Assess the morphology of the erythrocytes.
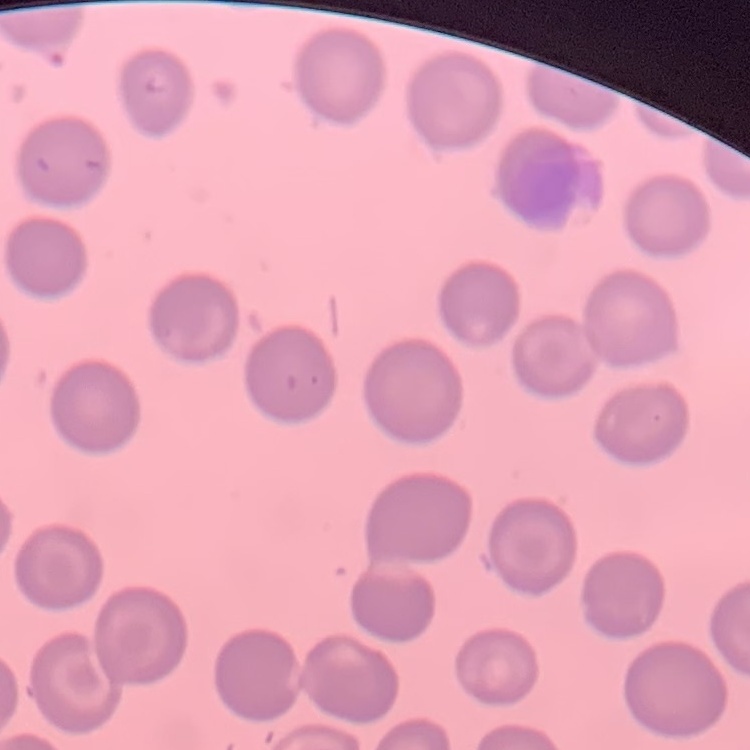
No rouleaux formation.

Thin peripheral smear. Stained with either Field's or Giemsa. One tile cut from a larger photomicrograph.